Identify the parasite.
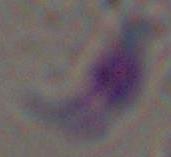

Toxoplasma gondii.

1000x magnification. Photomicrograph.